Comment on the morphology of the red blood cells.
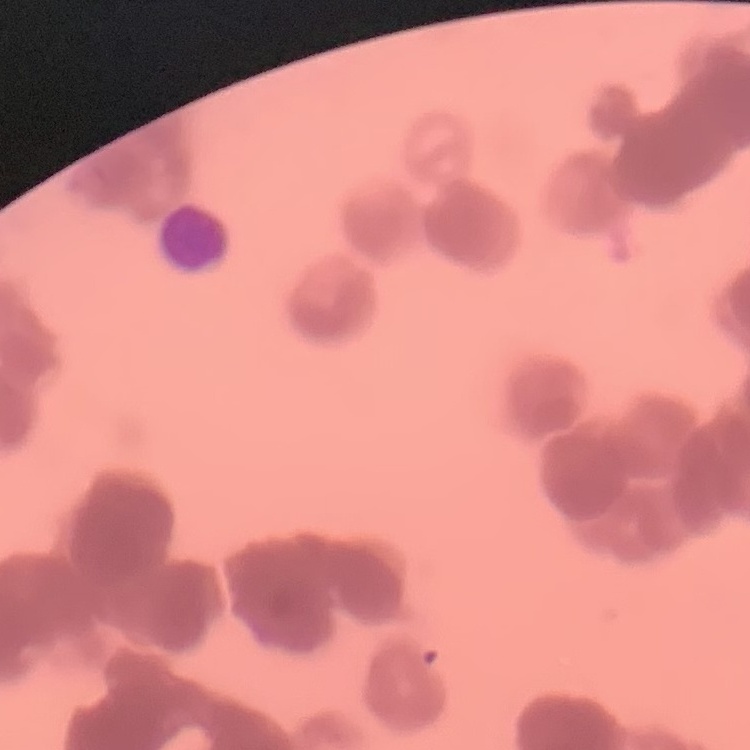

Rouleaux formation.

Stained with either Field's or Giemsa. Thin peripheral smear. One tile cut from a larger photomicrograph.